Assess the morphology of the red blood cells.
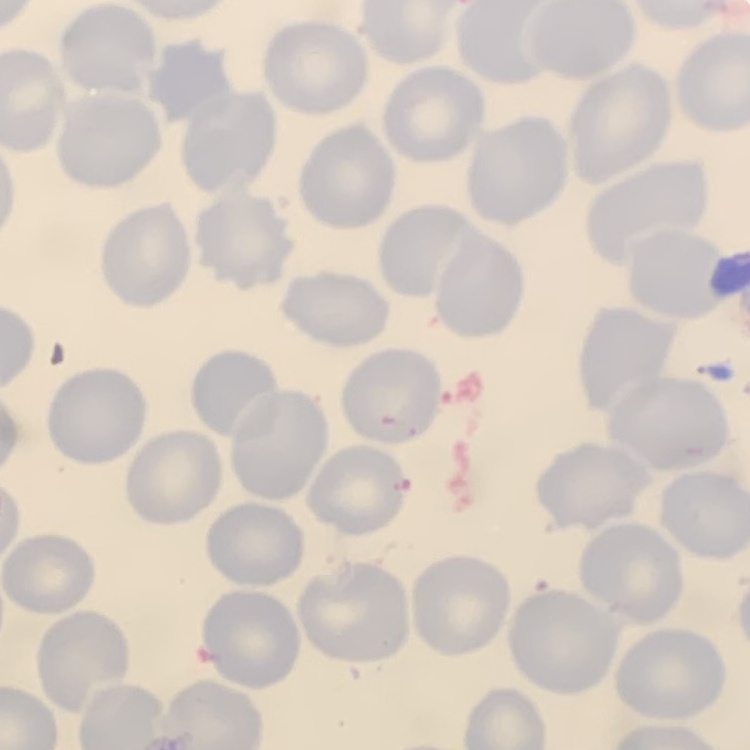
No rouleaux formation.

Thin blood film. One tile cut from a larger photomicrograph. Field's or Giemsa stain.